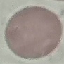
Summary:
  - Malaria status: uninfected
  - Capture: smartphone camera at the microscope eyepiece
  - Preparation: thin smear
  - Image type: automatically extracted cell patch, resized to 64 × 64 pixels
  - Stain: Giemsa